Identify the parasite.
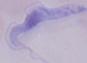

This is a trypanosome.

Summary:
  - Magnification: 1000x
  - Modality: micrograph